Locate every Plasmodium ovale-infected red blood cell.
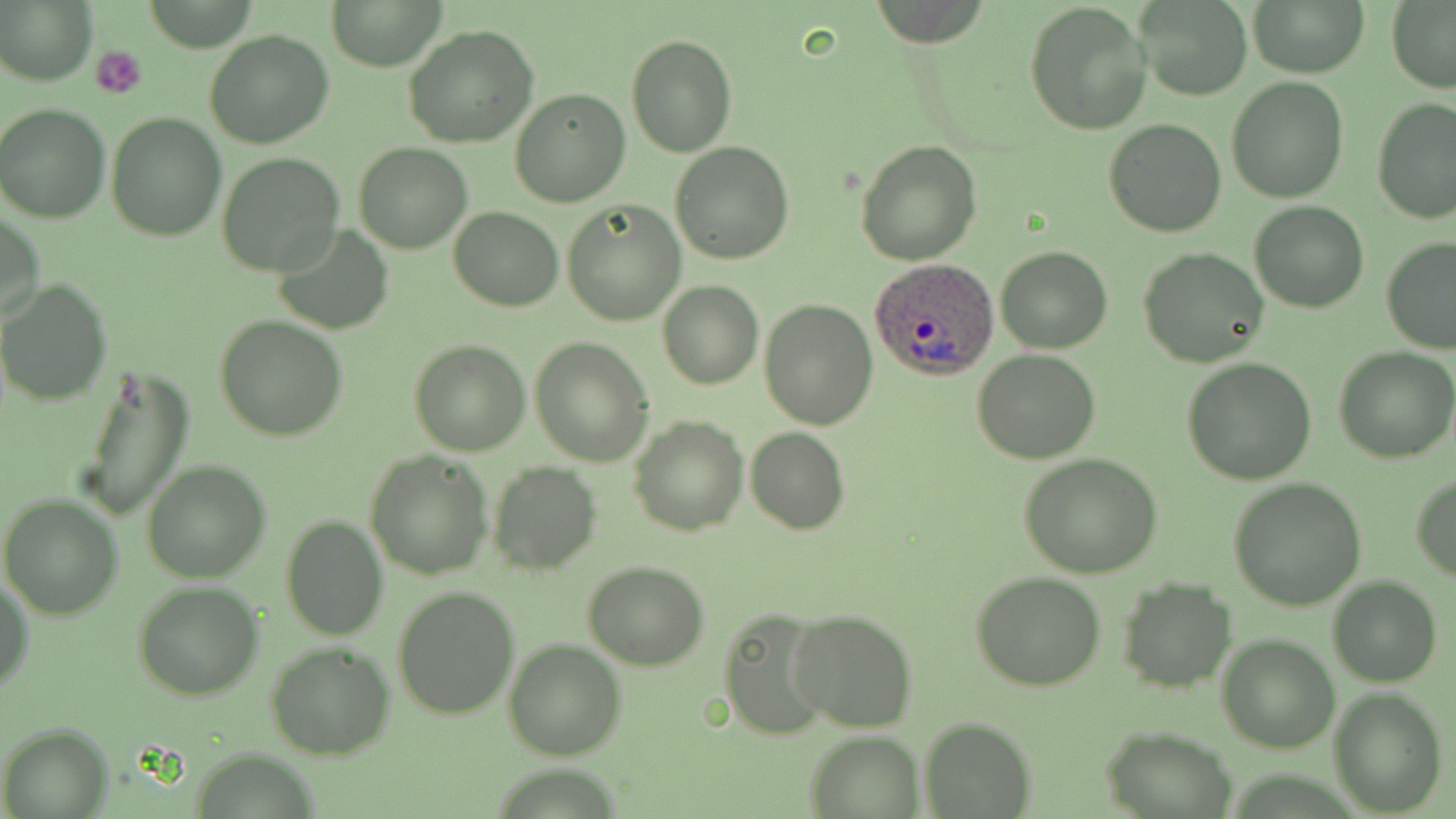
Approximate bounding boxes as named x1/y1/x2/y2 corners in pixels.
Plasmodium ovale-infected red blood cells: (x1=869, y1=259, x2=998, y2=379).

Summary:
  - Uninfected red blood cell locations: (x1=1, y1=0, x2=96, y2=85), (x1=327, y1=0, x2=447, y2=70), (x1=1024, y1=0, x2=1152, y2=136), (x1=1247, y1=0, x2=1369, y2=77), (x1=1137, y1=2, x2=1252, y2=101), (x1=1386, y1=3, x2=1456, y2=91), (x1=403, y1=24, x2=539, y2=150), (x1=205, y1=29, x2=334, y2=148), (x1=625, y1=33, x2=737, y2=157), (x1=1226, y1=77, x2=1350, y2=204), (x1=510, y1=89, x2=630, y2=207), (x1=1372, y1=99, x2=1455, y2=224), (x1=1, y1=102, x2=114, y2=222), (x1=106, y1=111, x2=229, y2=242), (x1=1103, y1=118, x2=1226, y2=236), (x1=856, y1=139, x2=981, y2=264), (x1=354, y1=142, x2=472, y2=254), (x1=670, y1=142, x2=794, y2=263), (x1=216, y1=153, x2=346, y2=276), (x1=563, y1=198, x2=687, y2=325), (x1=1248, y1=202, x2=1368, y2=314), (x1=448, y1=207, x2=563, y2=311), (x1=1, y1=211, x2=46, y2=325), (x1=274, y1=225, x2=393, y2=334), (x1=1381, y1=236, x2=1456, y2=354), (x1=997, y1=247, x2=1113, y2=354), (x1=1139, y1=248, x2=1269, y2=370), (x1=1, y1=279, x2=115, y2=406), (x1=658, y1=281, x2=763, y2=390), (x1=759, y1=298, x2=880, y2=429), (x1=214, y1=316, x2=348, y2=442), (x1=530, y1=337, x2=653, y2=465), (x1=409, y1=339, x2=529, y2=456), (x1=1334, y1=345, x2=1456, y2=463), (x1=972, y1=349, x2=1102, y2=464), (x1=1182, y1=357, x2=1316, y2=484), (x1=79, y1=364, x2=194, y2=525), (x1=629, y1=415, x2=748, y2=535), (x1=746, y1=427, x2=849, y2=534), (x1=365, y1=450, x2=493, y2=579), (x1=1018, y1=453, x2=1163, y2=577), (x1=141, y1=459, x2=272, y2=583), (x1=489, y1=461, x2=603, y2=576), (x1=1410, y1=474, x2=1456, y2=583), (x1=1229, y1=478, x2=1366, y2=610), (x1=0, y1=494, x2=124, y2=621), (x1=280, y1=516, x2=388, y2=641), (x1=584, y1=562, x2=710, y2=669), (x1=970, y1=571, x2=1106, y2=692), (x1=1329, y1=576, x2=1441, y2=688), (x1=0, y1=577, x2=33, y2=696), (x1=1117, y1=577, x2=1237, y2=693), (x1=133, y1=580, x2=263, y2=700), (x1=393, y1=585, x2=521, y2=720), (x1=718, y1=607, x2=838, y2=737), (x1=788, y1=608, x2=918, y2=733), (x1=1217, y1=636, x2=1339, y2=752), (x1=503, y1=639, x2=626, y2=761), (x1=264, y1=640, x2=395, y2=760), (x1=1328, y1=688, x2=1449, y2=816), (x1=919, y1=717, x2=1035, y2=819), (x1=4, y1=724, x2=110, y2=818), (x1=1100, y1=726, x2=1239, y2=818), (x1=804, y1=730, x2=925, y2=817)
  - Platelet locations: (x1=92, y1=45, x2=147, y2=99)
  - Slide-level diagnosis: Plasmodium ovale
  - Magnification: 1000x
  - Stain: May-Grünwald-Giemsa
  - Preparation: thin blood film
  - Image size: 1456×819 pixels
  - Modality: light microscopy
  - Field of view: single